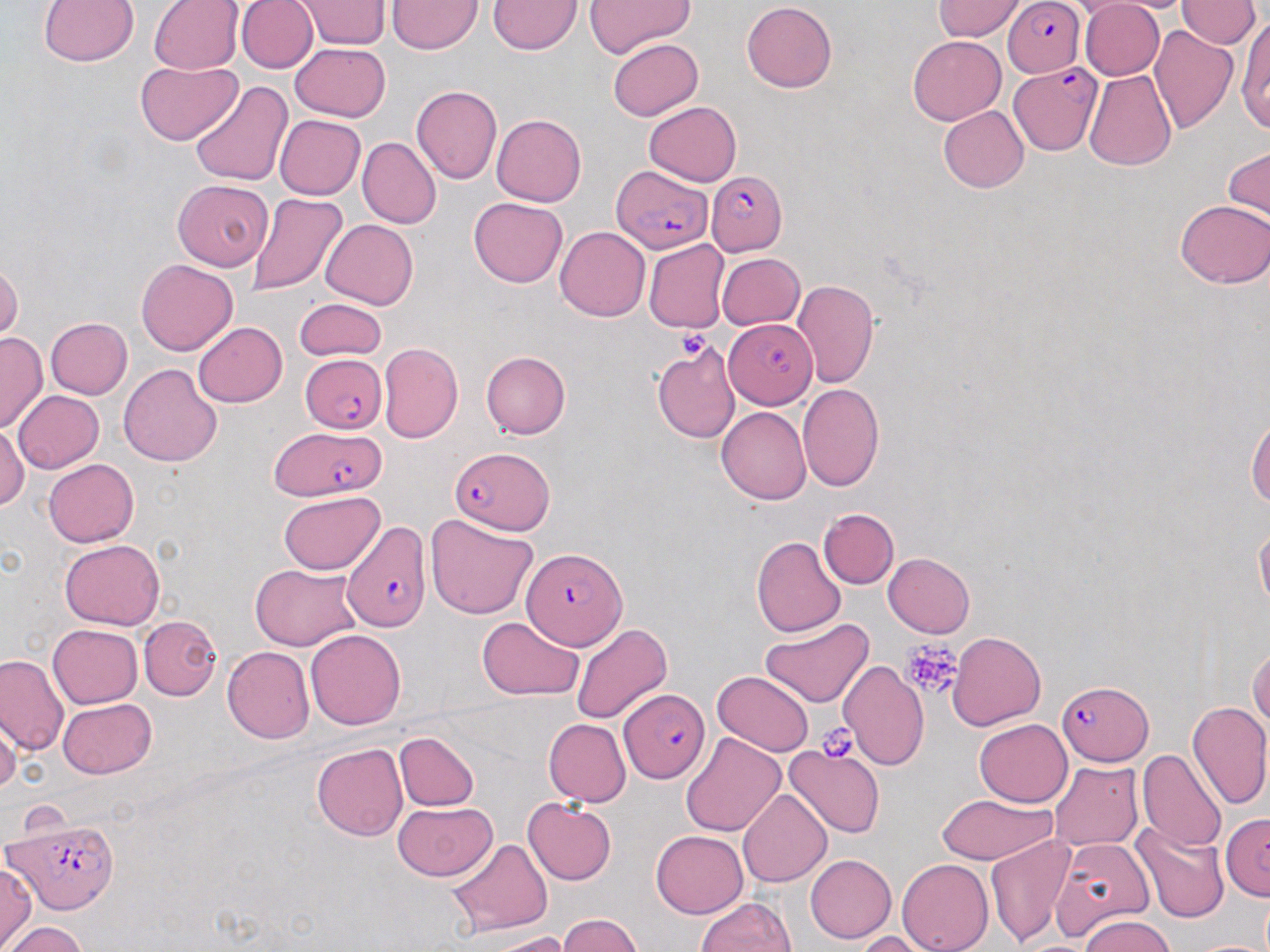

Summary:
  - Coordinate format: approximate bounding boxes as named x1/y1/x2/y2 corners in pixels
  - Platelet locations: (x1=675, y1=330, x2=710, y2=358), (x1=901, y1=641, x2=963, y2=699), (x1=814, y1=723, x2=863, y2=763)
  - Uninfected red blood cell locations: (x1=236, y1=0, x2=317, y2=72), (x1=294, y1=0, x2=392, y2=48), (x1=1079, y1=0, x2=1164, y2=81), (x1=1098, y1=0, x2=1201, y2=13), (x1=1176, y1=0, x2=1260, y2=48), (x1=37, y1=1, x2=140, y2=67), (x1=149, y1=1, x2=243, y2=74), (x1=386, y1=1, x2=482, y2=54), (x1=487, y1=1, x2=582, y2=54), (x1=583, y1=1, x2=694, y2=57), (x1=742, y1=1, x2=837, y2=93), (x1=933, y1=1, x2=1026, y2=41), (x1=1235, y1=15, x2=1270, y2=131), (x1=1149, y1=25, x2=1239, y2=134), (x1=908, y1=35, x2=1005, y2=124), (x1=606, y1=37, x2=702, y2=120), (x1=290, y1=43, x2=391, y2=121), (x1=135, y1=61, x2=242, y2=146), (x1=1084, y1=70, x2=1177, y2=170), (x1=189, y1=81, x2=294, y2=187), (x1=411, y1=85, x2=502, y2=184), (x1=644, y1=101, x2=742, y2=185), (x1=939, y1=106, x2=1029, y2=193), (x1=275, y1=114, x2=366, y2=199), (x1=492, y1=114, x2=587, y2=206), (x1=357, y1=137, x2=441, y2=229), (x1=1224, y1=146, x2=1269, y2=227), (x1=173, y1=180, x2=272, y2=271), (x1=247, y1=194, x2=348, y2=295), (x1=469, y1=198, x2=567, y2=287), (x1=1175, y1=200, x2=1270, y2=288), (x1=321, y1=219, x2=418, y2=309), (x1=555, y1=226, x2=649, y2=321), (x1=644, y1=239, x2=729, y2=333), (x1=717, y1=253, x2=804, y2=329), (x1=0, y1=257, x2=22, y2=345), (x1=136, y1=257, x2=237, y2=355), (x1=792, y1=278, x2=878, y2=388), (x1=294, y1=299, x2=386, y2=361), (x1=45, y1=317, x2=132, y2=399), (x1=194, y1=322, x2=287, y2=407), (x1=0, y1=331, x2=47, y2=433), (x1=651, y1=341, x2=741, y2=444), (x1=378, y1=342, x2=463, y2=443), (x1=481, y1=350, x2=571, y2=438), (x1=118, y1=363, x2=223, y2=468), (x1=797, y1=383, x2=885, y2=492), (x1=13, y1=391, x2=104, y2=473), (x1=717, y1=407, x2=811, y2=504), (x1=1247, y1=416, x2=1270, y2=508), (x1=0, y1=422, x2=29, y2=512), (x1=43, y1=458, x2=138, y2=547), (x1=279, y1=491, x2=385, y2=576), (x1=818, y1=508, x2=898, y2=589), (x1=425, y1=514, x2=539, y2=619), (x1=1254, y1=520, x2=1270, y2=611), (x1=750, y1=536, x2=845, y2=638), (x1=59, y1=538, x2=165, y2=630), (x1=883, y1=553, x2=975, y2=638), (x1=251, y1=563, x2=361, y2=650), (x1=476, y1=615, x2=584, y2=701), (x1=138, y1=616, x2=221, y2=699), (x1=761, y1=618, x2=873, y2=706), (x1=571, y1=623, x2=673, y2=724), (x1=48, y1=624, x2=144, y2=707), (x1=305, y1=628, x2=406, y2=729), (x1=947, y1=631, x2=1045, y2=730), (x1=1248, y1=645, x2=1269, y2=733), (x1=222, y1=646, x2=314, y2=743), (x1=0, y1=653, x2=68, y2=756), (x1=838, y1=659, x2=928, y2=768), (x1=712, y1=670, x2=814, y2=755), (x1=57, y1=697, x2=157, y2=779), (x1=1186, y1=699, x2=1270, y2=811), (x1=0, y1=714, x2=21, y2=797), (x1=544, y1=719, x2=631, y2=806), (x1=974, y1=719, x2=1073, y2=807), (x1=393, y1=731, x2=479, y2=811), (x1=681, y1=731, x2=785, y2=836), (x1=311, y1=743, x2=408, y2=841), (x1=783, y1=743, x2=886, y2=838), (x1=1137, y1=749, x2=1227, y2=852), (x1=1050, y1=761, x2=1144, y2=851), (x1=738, y1=789, x2=832, y2=887), (x1=937, y1=793, x2=1057, y2=864), (x1=523, y1=799, x2=616, y2=885), (x1=393, y1=802, x2=496, y2=881), (x1=1133, y1=821, x2=1228, y2=923), (x1=651, y1=831, x2=747, y2=917), (x1=987, y1=833, x2=1075, y2=948), (x1=1051, y1=836, x2=1155, y2=939), (x1=447, y1=838, x2=553, y2=935), (x1=805, y1=854, x2=896, y2=943), (x1=897, y1=857, x2=993, y2=952), (x1=0, y1=861, x2=36, y2=951), (x1=695, y1=897, x2=795, y2=952), (x1=557, y1=913, x2=643, y2=951), (x1=1080, y1=913, x2=1175, y2=951), (x1=2, y1=922, x2=88, y2=952), (x1=484, y1=931, x2=571, y2=952), (x1=853, y1=931, x2=937, y2=952)
  - Plasmodium falciparum-infected red blood cell locations: (x1=1004, y1=1, x2=1085, y2=78), (x1=1009, y1=63, x2=1098, y2=157), (x1=613, y1=164, x2=715, y2=257), (x1=707, y1=168, x2=786, y2=255), (x1=724, y1=317, x2=817, y2=407), (x1=300, y1=354, x2=386, y2=433), (x1=270, y1=425, x2=384, y2=501), (x1=450, y1=447, x2=554, y2=534), (x1=341, y1=520, x2=432, y2=632), (x1=522, y1=548, x2=625, y2=650), (x1=1057, y1=680, x2=1152, y2=764), (x1=621, y1=688, x2=710, y2=783), (x1=5, y1=813, x2=118, y2=914), (x1=1219, y1=813, x2=1270, y2=900)
  - Slide-level diagnosis: Plasmodium falciparum
  - Preparation: thin blood smear
  - Field of view: single
  - Modality: optical microscopy
  - Image size: 1270×952 pixels
  - Stain: May-Grünwald-Giemsa
  - Magnification: 1000x